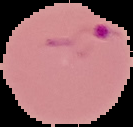
Image is 133×127 pixels. Result: malaria parasites detected. From a thin blood smear. Cell region segmented out of the field of view; the surrounding area is masked to black.